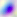 400x magnification. Toxoplasma gondii is shown. Photomicrograph.